Evaluate for malaria.
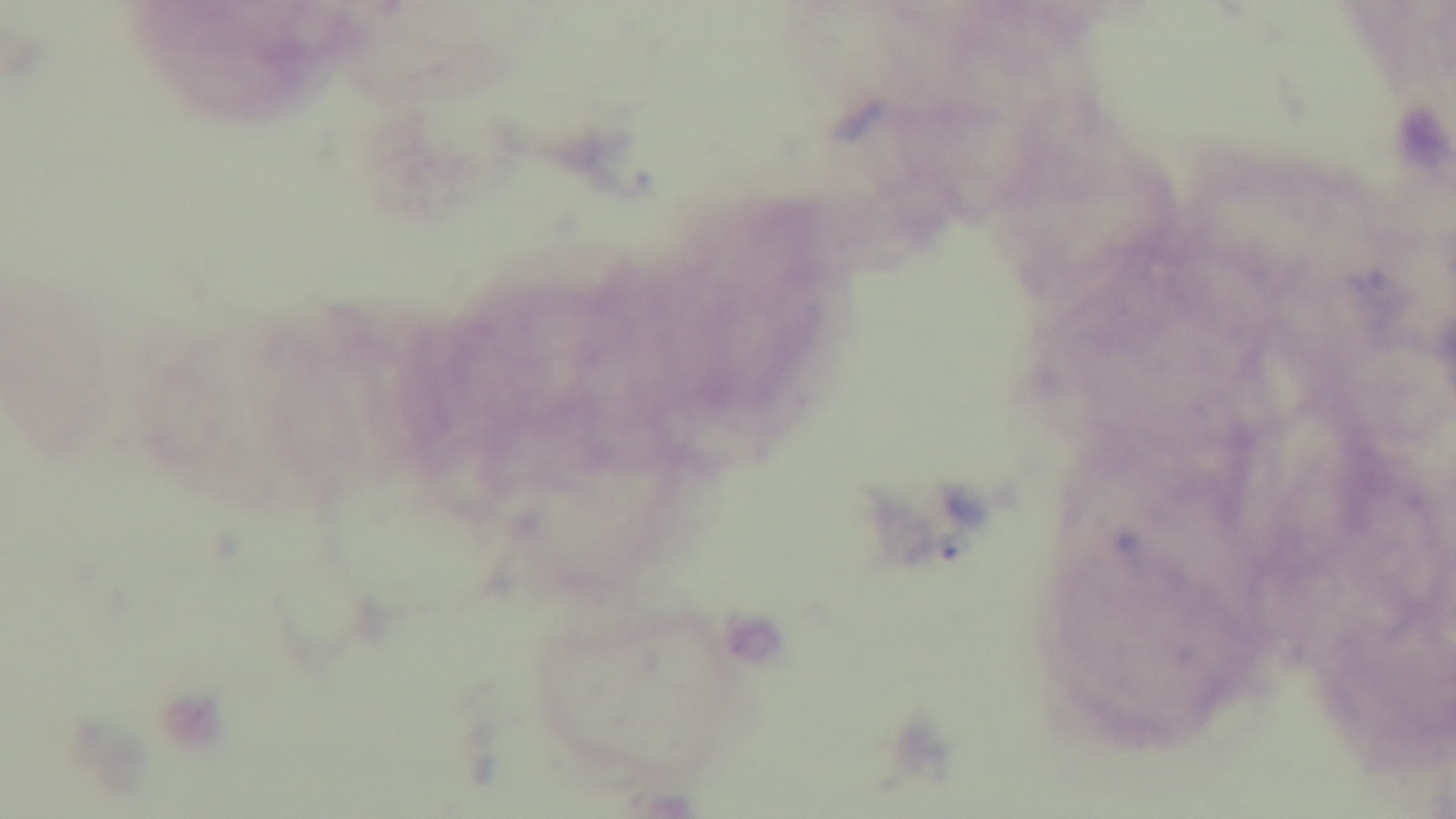

Negative.

Summary:
  - Preparation: thick
  - Objective: 100x oil immersion
  - Modality: light microscopy
  - Field of view: single
  - Stain: Giemsa
  - Capture: mounted 4K digital camera